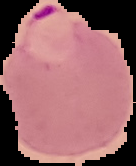

Summary:
  - Preparation: thin blood smear
  - Image type: cell region segmented out of the field of view; surrounding area masked to black
  - Result: malaria parasites detected
  - Image size: 136×166 pixels